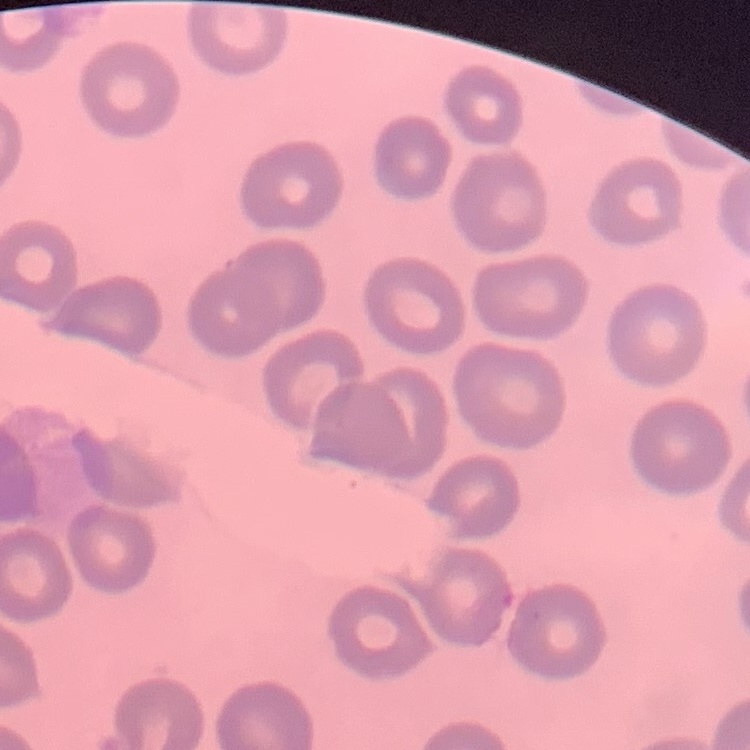

Summary:
  - Red blood cell morphology: no rouleaux formation
  - Stain: Field's or Giemsa
  - Image type: square crop of a larger photomicrograph
  - Preparation: thin peripheral smear